Report the malaria status of this cell.
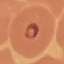
It is parasitized.

Giemsa stain. Cell patch, automatically extracted from a larger field of view and resized to 64 × 64 pixels. Acquired by smartphone through the microscope eyepiece. Thin blood smear.